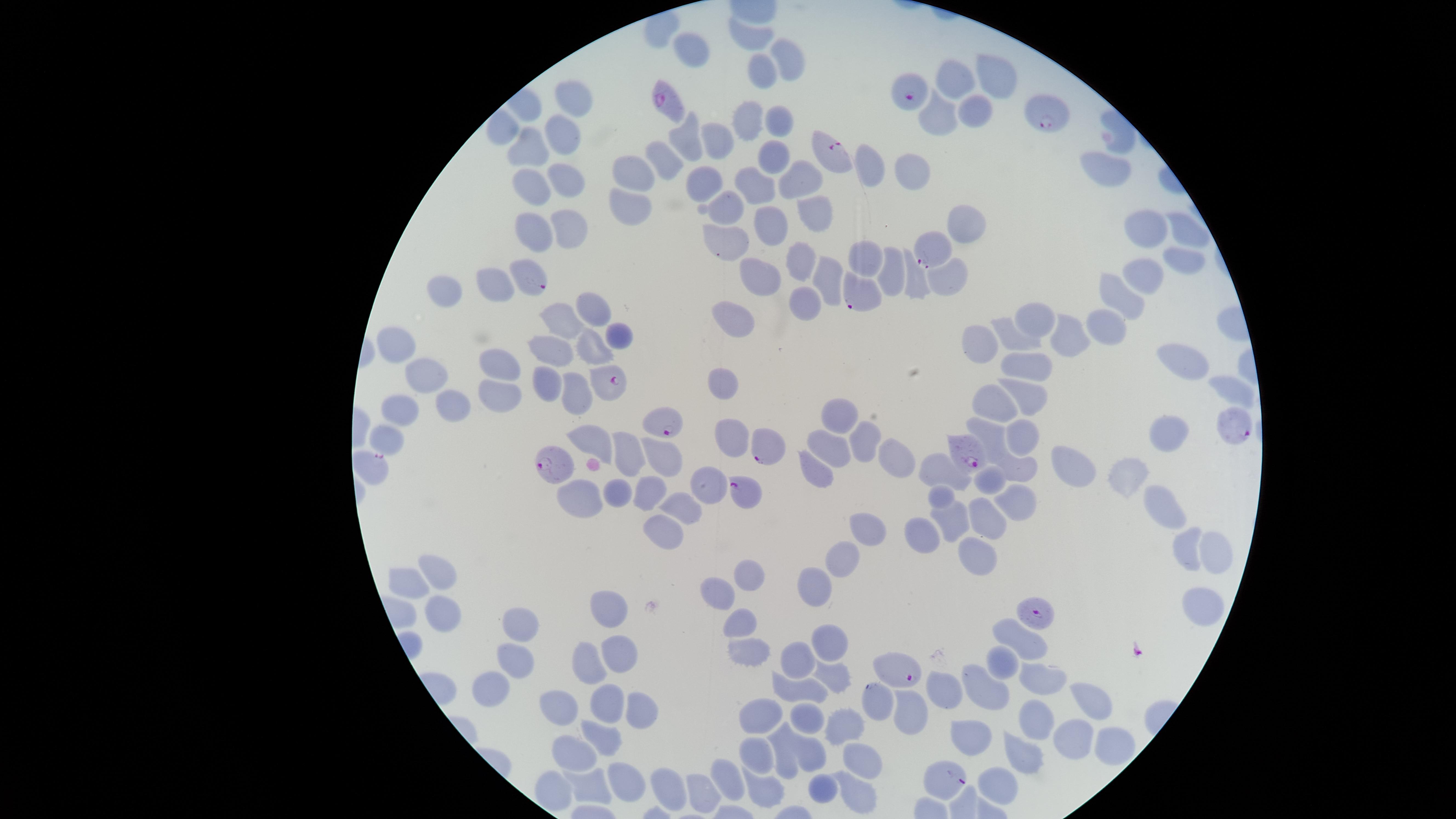

Approximate marker points as (x, y) in pixels.
Summary:
  - Uninfected RBCs: (754, 34), (690, 49), (787, 57), (765, 77), (990, 78), (955, 81), (570, 100), (975, 106), (938, 116), (780, 118), (751, 122), (501, 132), (686, 137), (566, 141), (716, 141), (773, 150), (524, 153), (665, 156), (875, 165), (1101, 170), (917, 171), (637, 172), (801, 175), (566, 183), (705, 183), (758, 188), (531, 191), (726, 204), (628, 207), (809, 212), (566, 226), (771, 226), (965, 226), (1142, 230), (533, 231), (1187, 233), (727, 245), (867, 257), (1182, 258), (801, 259), (884, 271), (761, 276), (1144, 277), (828, 280), (494, 283), (950, 285), (914, 288), (444, 293), (1127, 294), (809, 302), (594, 309), (737, 316), (1035, 319), (1109, 326), (561, 327), (610, 334), (1076, 338), (1015, 342), (396, 346), (979, 347), (592, 351), (548, 356), (1177, 358), (499, 364), (1033, 365), (431, 374), (723, 384), (545, 385), (1225, 387), (576, 392), (497, 394), (1028, 399), (999, 403), (453, 407), (400, 410), (845, 414), (731, 431), (990, 433), (1021, 436), (868, 439), (387, 440), (1170, 440), (601, 442), (831, 448), (633, 458), (894, 461), (1070, 465), (668, 466), (812, 468), (1016, 469), (946, 471), (1125, 475), (991, 482), (616, 487), (703, 487), (646, 490), (944, 496), (588, 501), (682, 505), (1015, 506), (1166, 506), (950, 519), (987, 520), (869, 525), (664, 533), (925, 535), (1185, 548), (1218, 552), (979, 554), (845, 556), (751, 571), (438, 577), (407, 582), (818, 588), (723, 597), (1203, 597), (442, 610), (608, 611), (519, 623), (739, 624), (1021, 638), (828, 647), (620, 652), (749, 653), (513, 654), (1004, 660), (791, 661), (588, 666), (1044, 679), (828, 681), (497, 684), (799, 690), (947, 691), (983, 691), (1093, 697), (607, 707), (915, 708), (563, 709), (768, 712), (639, 713), (807, 719), (1041, 720), (838, 721), (980, 739), (606, 741), (1071, 745), (1117, 745), (757, 750), (1027, 753), (573, 755), (810, 756), (786, 759), (866, 761), (622, 779), (730, 780), (669, 784), (1000, 784), (824, 789), (589, 790), (762, 790), (705, 795), (860, 799)
  - Parasitized RBCs: (906, 90), (666, 99), (1049, 114), (831, 151), (930, 248), (535, 281), (855, 294), (604, 380), (665, 426), (1235, 427), (769, 442), (967, 450), (555, 465), (373, 467), (746, 494), (1039, 611), (900, 674), (875, 703), (947, 780)
  - Capture: smartphone photograph through the microscope eyepiece
  - Visible region: circular
  - Field of view: single
  - Presence: malaria parasites seen
  - Species: Plasmodium falciparum
  - Image size: 1456×819 pixels
  - Preparation: thin smear of blood
  - Stain: Giemsa